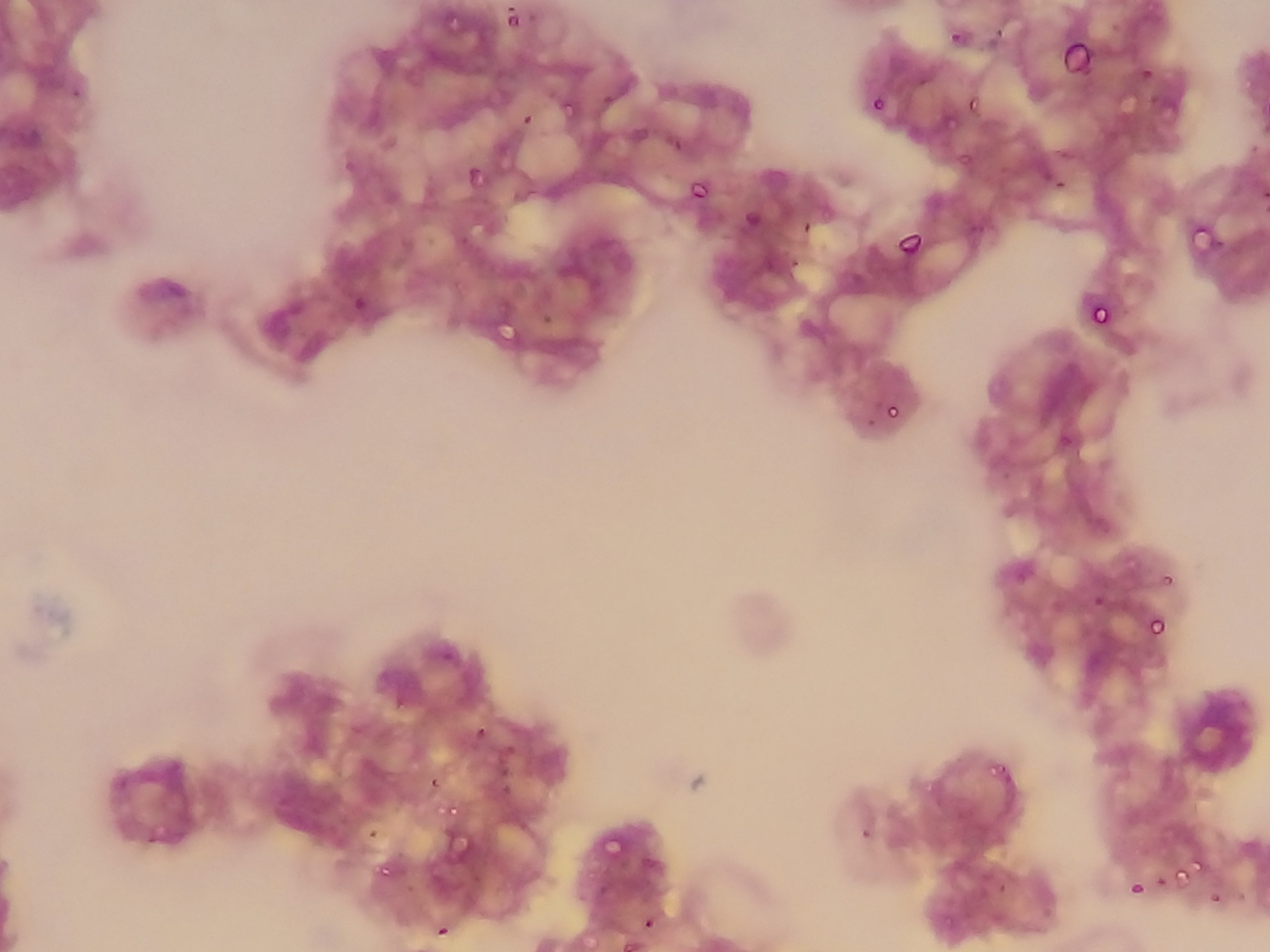
Approximate bounding boxes as {left, top, right, bottom} in pixels. Malaria parasite locations: {503, 7, 523, 25}, {442, 8, 461, 29}, {526, 9, 540, 26}, {995, 25, 1011, 47}, {949, 29, 965, 45}, {1058, 37, 1093, 76}, {1129, 68, 1160, 85}, {1116, 83, 1143, 113}, {596, 90, 618, 107}, {1143, 91, 1163, 108}, {869, 96, 885, 113}, {559, 97, 575, 115}, {965, 97, 980, 111}, {512, 105, 538, 136}, {660, 122, 685, 152}, {489, 148, 509, 175}, {957, 150, 973, 167}, {463, 164, 485, 186}, {1038, 165, 1078, 187}, {689, 177, 710, 202}, {744, 210, 760, 225}, {795, 218, 822, 240}, {1193, 222, 1228, 258}, {896, 229, 923, 256}, {456, 235, 469, 248}, {785, 252, 806, 279}, {353, 294, 367, 309}, {1089, 303, 1110, 327}, {540, 311, 554, 327}, {492, 312, 519, 348}, {883, 399, 902, 420}, {864, 414, 876, 426}, {1058, 431, 1077, 450}, {1091, 594, 1105, 609}, {1146, 613, 1166, 636}, {435, 645, 464, 662}, {392, 698, 408, 712}, {348, 721, 367, 739}, {472, 725, 491, 741}, {486, 733, 520, 774}, {987, 760, 1007, 779}, {428, 776, 440, 791}, {502, 789, 514, 804}, {441, 817, 476, 859}, {359, 818, 385, 840}, {858, 826, 872, 842}, {598, 832, 626, 859}, {377, 862, 392, 878}, {1173, 866, 1190, 884}, {1153, 875, 1169, 889}, {1127, 879, 1145, 897}, {995, 880, 1009, 896}, {1209, 891, 1222, 905}, {641, 916, 654, 932}, {434, 922, 451, 939}. Sample from Ghana. Mobile-phone photograph taken through the microscope. Single field of view. Thin blood film. Image is 1270×952 pixels.